Locate the cells, classifying each as a parasitized red blood cell, an uninfected red blood cell, or a white blood cell.
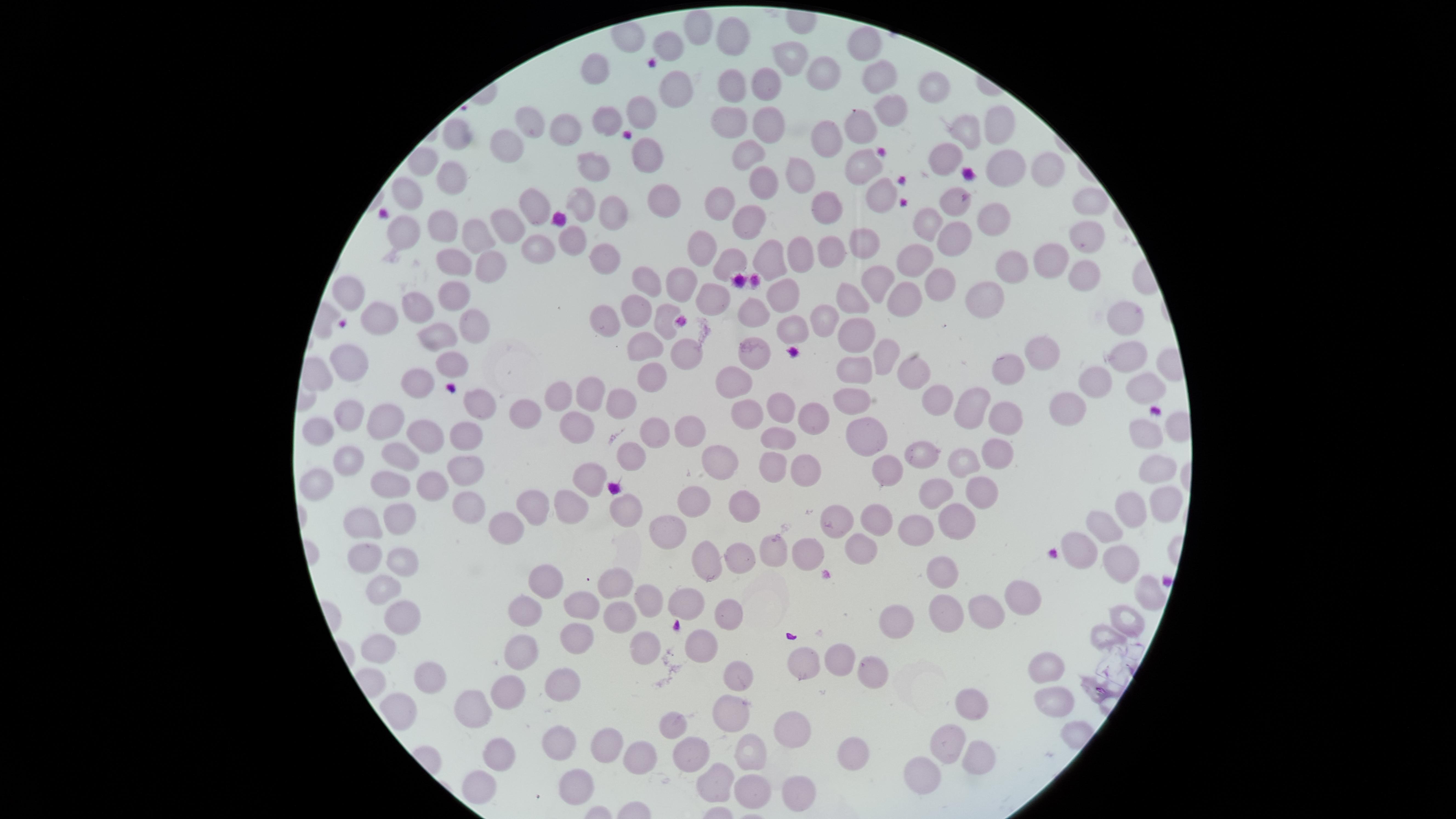

No parasitized red blood cells identified.
Approximate marker points as (x, y) in pixels.
Uninfected red blood cells: (702, 24), (735, 37), (668, 42), (867, 45), (786, 56), (600, 69), (823, 69), (879, 73), (762, 82), (936, 82), (678, 84), (735, 84), (893, 105), (641, 113), (733, 114), (531, 115), (608, 116), (767, 122), (995, 125), (861, 128), (966, 129), (566, 130), (460, 132), (826, 138), (506, 141), (648, 155), (750, 155), (947, 155), (597, 166), (864, 166), (1006, 166), (1044, 168), (450, 174), (795, 174), (764, 182), (410, 191), (662, 193), (883, 193), (955, 195), (580, 196), (722, 200), (531, 203), (1093, 203), (828, 207), (618, 215), (753, 217), (996, 219), (926, 220), (508, 222), (441, 225), (407, 227), (478, 233), (1086, 233), (956, 237), (573, 239), (538, 244), (868, 245), (708, 246), (831, 251), (609, 255), (734, 257), (771, 257), (798, 257), (913, 258), (1048, 258), (454, 259), (485, 265), (1012, 268), (1087, 271), (643, 278), (876, 278), (940, 279), (679, 286), (349, 292), (781, 293), (455, 294), (900, 294), (712, 295), (986, 296), (851, 303), (414, 306), (754, 310), (635, 311), (1123, 313), (826, 314), (384, 315), (666, 318), (473, 320), (609, 323), (797, 326), (856, 331), (435, 333), (640, 345), (758, 355), (684, 356), (1048, 357), (1127, 357), (883, 358), (455, 363), (348, 366), (1011, 367), (918, 368), (853, 371), (650, 375), (734, 381), (420, 384), (1098, 385), (1151, 389), (588, 391), (853, 391), (561, 394), (941, 395), (479, 396), (623, 401), (1072, 404), (775, 405), (976, 405), (529, 408), (349, 410), (752, 411), (1013, 415), (811, 416), (387, 420), (323, 422), (567, 426), (655, 429), (687, 429), (870, 432), (781, 434), (1152, 434), (460, 436), (422, 437), (401, 448), (927, 450), (994, 454), (637, 455), (349, 458), (721, 458), (970, 459), (773, 463), (467, 464), (1158, 466), (806, 469), (881, 469), (589, 478), (313, 481), (394, 483), (428, 483), (934, 491), (979, 491), (573, 497), (692, 498), (472, 500), (628, 501), (531, 503), (746, 503), (1164, 507), (1128, 508), (876, 514), (402, 516), (955, 516), (840, 517), (359, 518), (1110, 520), (509, 522), (668, 525), (917, 527), (855, 546), (1080, 547), (805, 549), (772, 553), (367, 555), (737, 557), (1115, 557), (708, 561), (405, 562), (944, 563), (548, 573), (610, 580), (383, 584), (1026, 597), (641, 598), (687, 598), (584, 600), (522, 604), (984, 607), (727, 614), (901, 615), (941, 615), (401, 616), (614, 617), (1128, 619), (1109, 633), (571, 639), (702, 641), (381, 646), (642, 648), (839, 651), (526, 653), (803, 658), (876, 662), (1048, 667), (735, 673), (421, 677), (563, 685), (512, 687), (473, 697), (1049, 697), (971, 700), (723, 712), (674, 722), (799, 728), (949, 736), (604, 740), (558, 741), (499, 750), (698, 750), (744, 750), (852, 752), (638, 754), (977, 754), (913, 765), (716, 776), (576, 777), (473, 782), (794, 783), (751, 785).
No white blood cells identified.

The visible region is circular. Giemsa stain. Thin smear of blood. One field of view of the specimen. Photographed with a smartphone camera through the microscope eyepiece. Image is 1456×819 pixels.